Name the cell type shown.
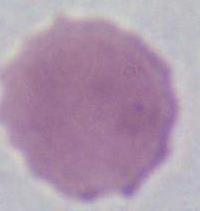

This is an erythrocyte.

magnification = 1000x
modality = micrograph